Assess this cell for malaria.
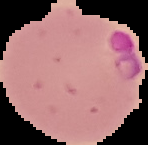

Parasitized.

Summary:
  - Image size: 148×145 pixels
  - Preparation: thin blood smear
  - Image type: segmented cell region on a black background